State which parasite is depicted.
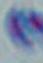

This is Toxoplasma gondii.

{
  "magnification": "1000x",
  "modality": "photomicrograph"
}